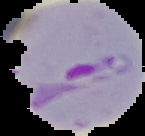
Summary:
  - Result: Plasmodium parasites identified
  - Image size: 145×136 pixels
  - Preparation: thin blood smear
  - Image type: segmented cell region on a black background